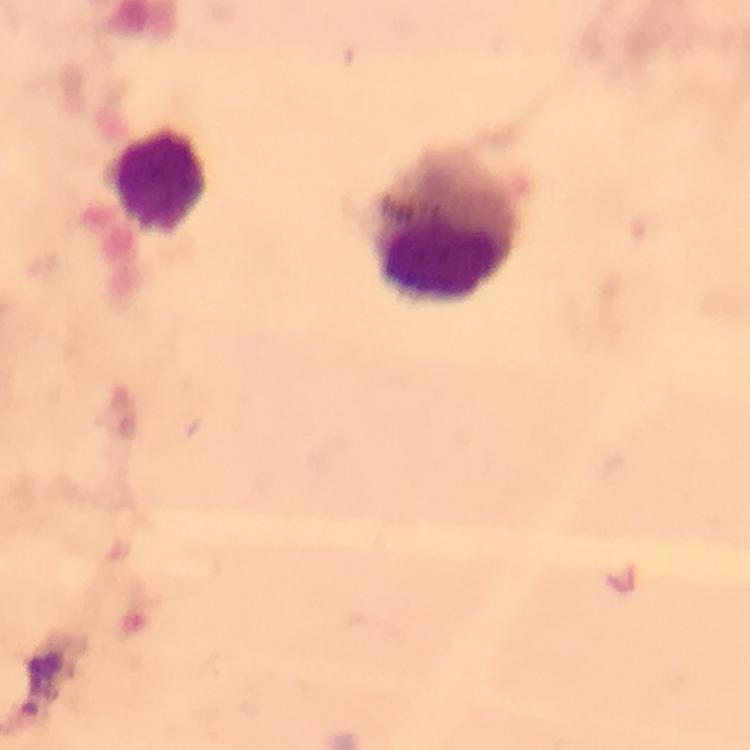
Approximate centers as [x, y] in pixels.
Summary:
  - Leukocyte locations: [160, 179], [443, 221]
  - Image size: 750×750 pixels
  - Capture: smartphone mounted on the microscope
  - Magnification: 100x
  - Cropped from: one field of view
  - Context: from a malaria diagnostic workup
  - Plasmodium parasites: none detected
  - Preparation: thick blood film
  - Stain: Giemsa
  - Immersion oil: used